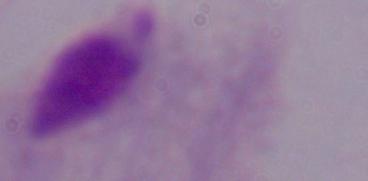
Micrograph. Captured at 1000x magnification. A trichomonad is shown.